Classify this cell by malaria status.
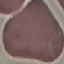

It is uninfected.

stain = Giemsa
preparation = thin blood film
image type = cell patch, automatically extracted from a larger field of view and resized to 64 × 64 pixels
capture = smartphone camera at the microscope eyepiece